Point out each malaria parasite.
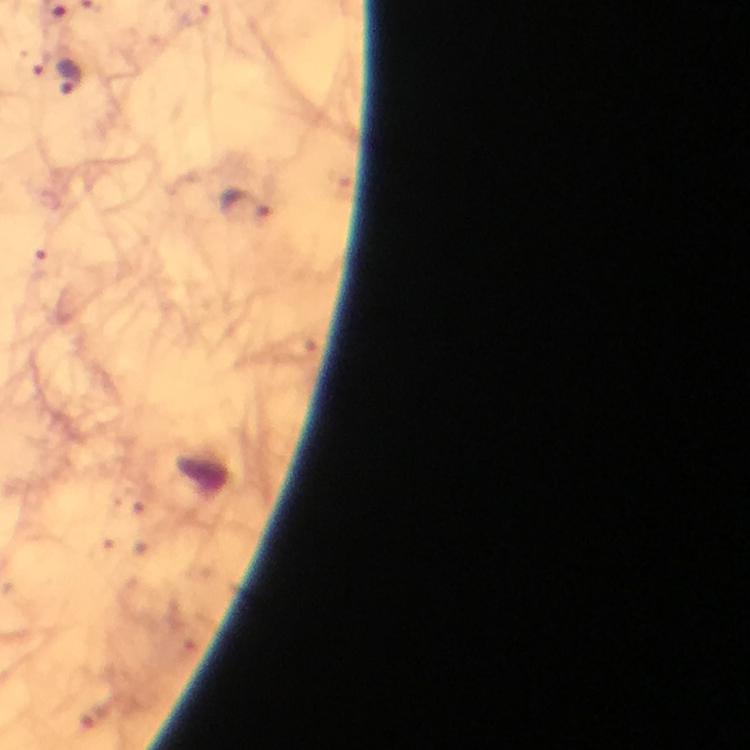
Approximate centers as (x, y) in pixels.
Malaria parasites: (69, 76), (242, 204).

Summary:
  - Image size: 750×750 pixels
  - Stain: Giemsa
  - Capture: smartphone photograph through a microscope
  - Context: from a malaria diagnostic workup
  - Magnification: 100x
  - Preparation: thick blood film
  - Cropped from: one field of view
  - Immersion oil: used